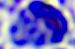

modality = photomicrograph
identification = leukocyte
magnification = 400x